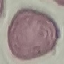
Summary:
  - Result: no malaria parasites detected
  - Capture: smartphone through the microscope eyepiece
  - Stain: Giemsa
  - Preparation: thin blood smear
  - Image type: cell patch, automatically extracted from a larger field of view and resized to 64 × 64 pixels